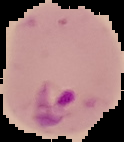

image type = cell region segmented out of the field of view; surrounding area masked to black
preparation = thin blood film
image size = 124×142 pixels
malaria status = parasitized